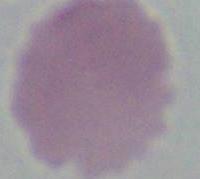
magnification = 1000x
identification = erythrocyte
modality = micrograph